Report the malaria status of this cell.
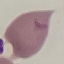

It is uninfected.

Thin blood smear. Automatically extracted cell patch, resized to 64 × 64 pixels. Acquired by smartphone through the microscope eyepiece. Giemsa-stained preparation.